Outline each blood parasite and name the species.
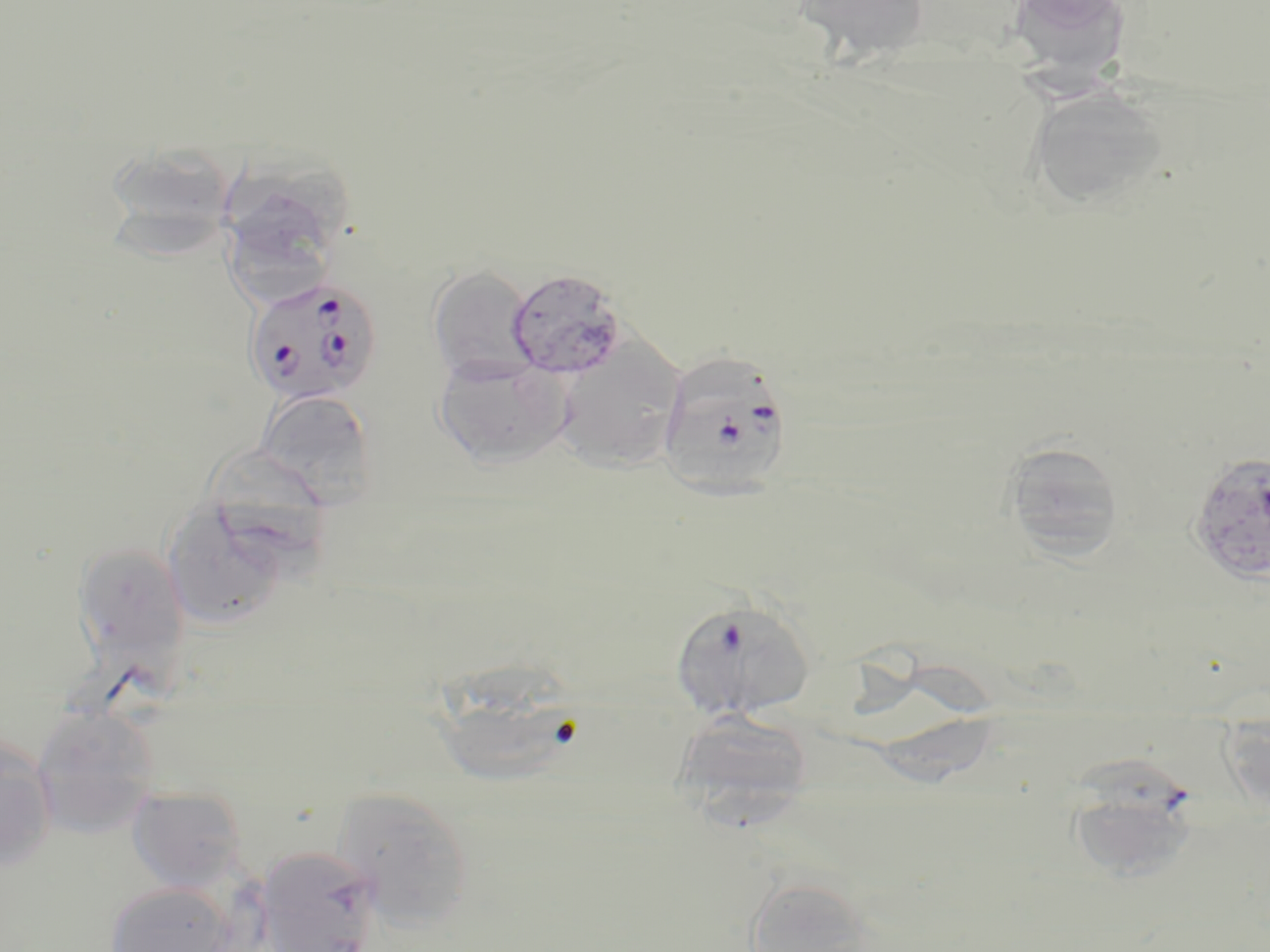

Approximate bounding boxes as named x1/y1/x2/y2 corners in pixels.
Plasmodium falciparum-infected red blood cells: (x1=237, y1=279, x2=377, y2=409), (x1=657, y1=351, x2=793, y2=501), (x1=1192, y1=452, x2=1270, y2=586), (x1=669, y1=597, x2=816, y2=721), (x1=1064, y1=765, x2=1202, y2=883).
No Plasmodium ovale, Plasmodium malariae, Plasmodium vivax, Babesia divergens, or Trypanosoma brucei observed.

Summary:
  - Uninfected red blood cell locations: (x1=791, y1=0, x2=931, y2=65), (x1=1006, y1=0, x2=1133, y2=77), (x1=1024, y1=85, x2=1171, y2=212), (x1=100, y1=140, x2=241, y2=253), (x1=225, y1=157, x2=356, y2=245), (x1=222, y1=204, x2=334, y2=302), (x1=427, y1=265, x2=538, y2=384), (x1=506, y1=268, x2=627, y2=379), (x1=549, y1=339, x2=688, y2=475), (x1=433, y1=353, x2=571, y2=468), (x1=255, y1=389, x2=378, y2=505), (x1=1000, y1=439, x2=1126, y2=561), (x1=213, y1=442, x2=336, y2=559), (x1=161, y1=501, x2=292, y2=634), (x1=73, y1=541, x2=191, y2=669), (x1=430, y1=653, x2=585, y2=785), (x1=30, y1=704, x2=161, y2=839), (x1=674, y1=706, x2=815, y2=822), (x1=0, y1=738, x2=57, y2=872), (x1=126, y1=786, x2=248, y2=894), (x1=331, y1=786, x2=476, y2=928), (x1=254, y1=845, x2=383, y2=952), (x1=742, y1=874, x2=883, y2=952), (x1=104, y1=880, x2=243, y2=952)
  - Slide-level diagnosis: Plasmodium falciparum
  - Stain: May-Grünwald-Giemsa
  - Image size: 1270×952 pixels
  - Modality: light microscopy
  - Magnification: 1000x
  - Field of view: single
  - Preparation: thin blood film